Locate every Plasmodium parasite.
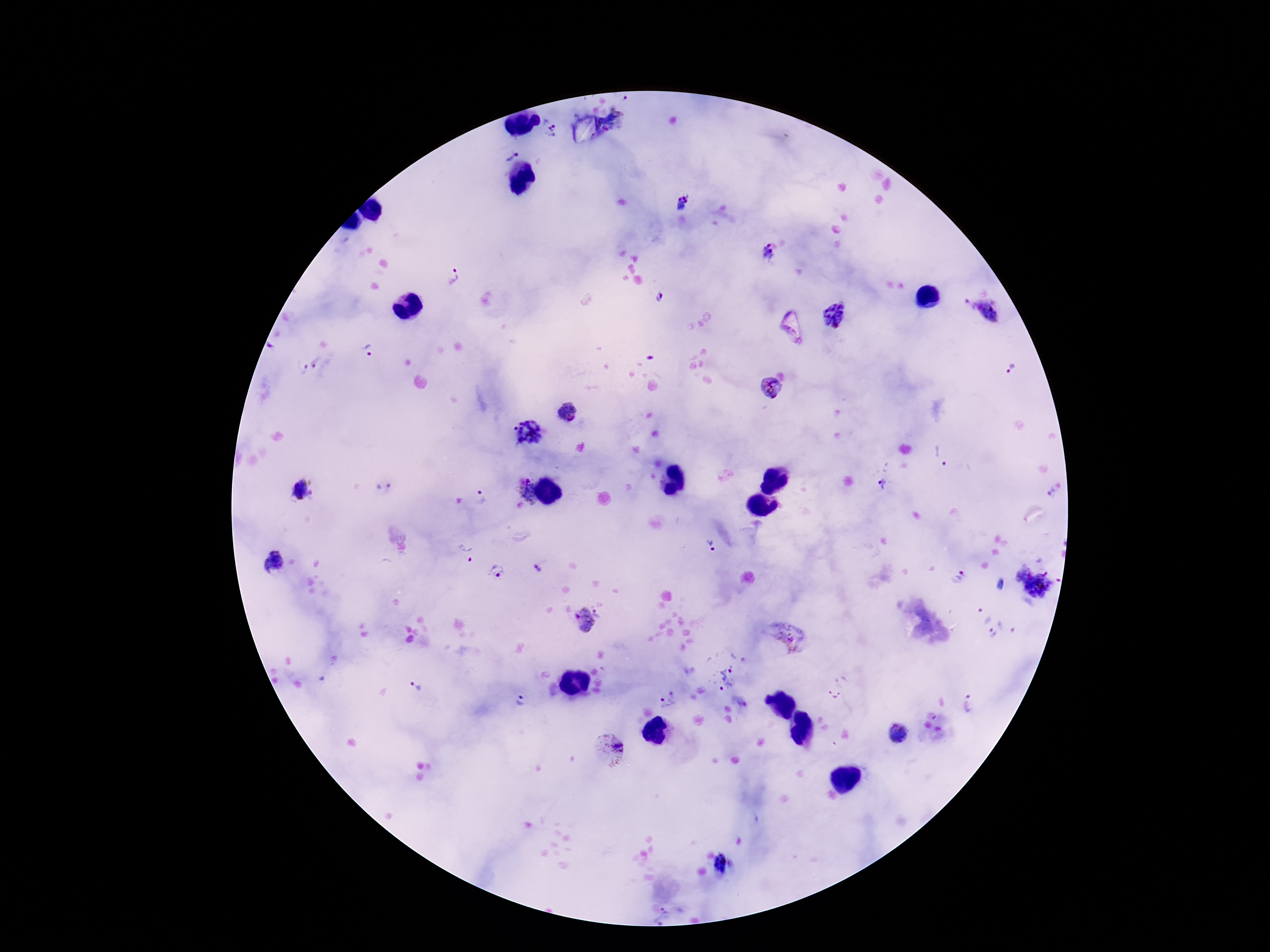
Approximate object centers, in pixels from the top-left corner.
Plasmodium parasites: (x=549, y=127), (x=509, y=149), (x=681, y=205), (x=768, y=254), (x=451, y=276), (x=660, y=298), (x=982, y=312), (x=834, y=317), (x=369, y=352), (x=308, y=366), (x=1013, y=371), (x=771, y=389), (x=569, y=412), (x=529, y=435), (x=942, y=458), (x=885, y=481), (x=383, y=488), (x=299, y=492), (x=523, y=492), (x=1050, y=493), (x=482, y=496), (x=709, y=546), (x=465, y=554), (x=279, y=562), (x=542, y=566), (x=1019, y=570), (x=497, y=573), (x=957, y=577), (x=999, y=584), (x=1040, y=586), (x=982, y=614), (x=586, y=621), (x=993, y=633), (x=788, y=636), (x=720, y=678), (x=415, y=685), (x=837, y=687), (x=665, y=698), (x=516, y=702), (x=970, y=705), (x=898, y=732), (x=608, y=749), (x=722, y=864), (x=661, y=917).

Summary:
  - Preparation: thick peripheral-blood smear
  - Magnification: 100x
  - Capture: smartphone camera through the microscope eyepiece
  - Field of view: one from this slide
  - Image size: 1270×952 pixels
  - Patient malaria status: positive
  - Stain: Giemsa